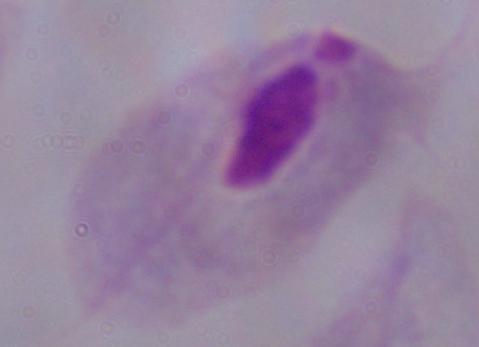
Photomicrograph. A trichomonad is shown. 1000x magnification.